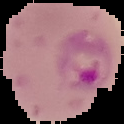

{
  "preparation": "thin blood smear",
  "image_type": "segmented cell region on a black background",
  "image_size": "124×124 pixels",
  "result": "Plasmodium parasites detected"
}